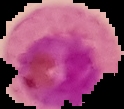

Segmented cell region on a black background. From a thin blood smear. Image is 124×109 pixels. Result: malaria parasites detected.